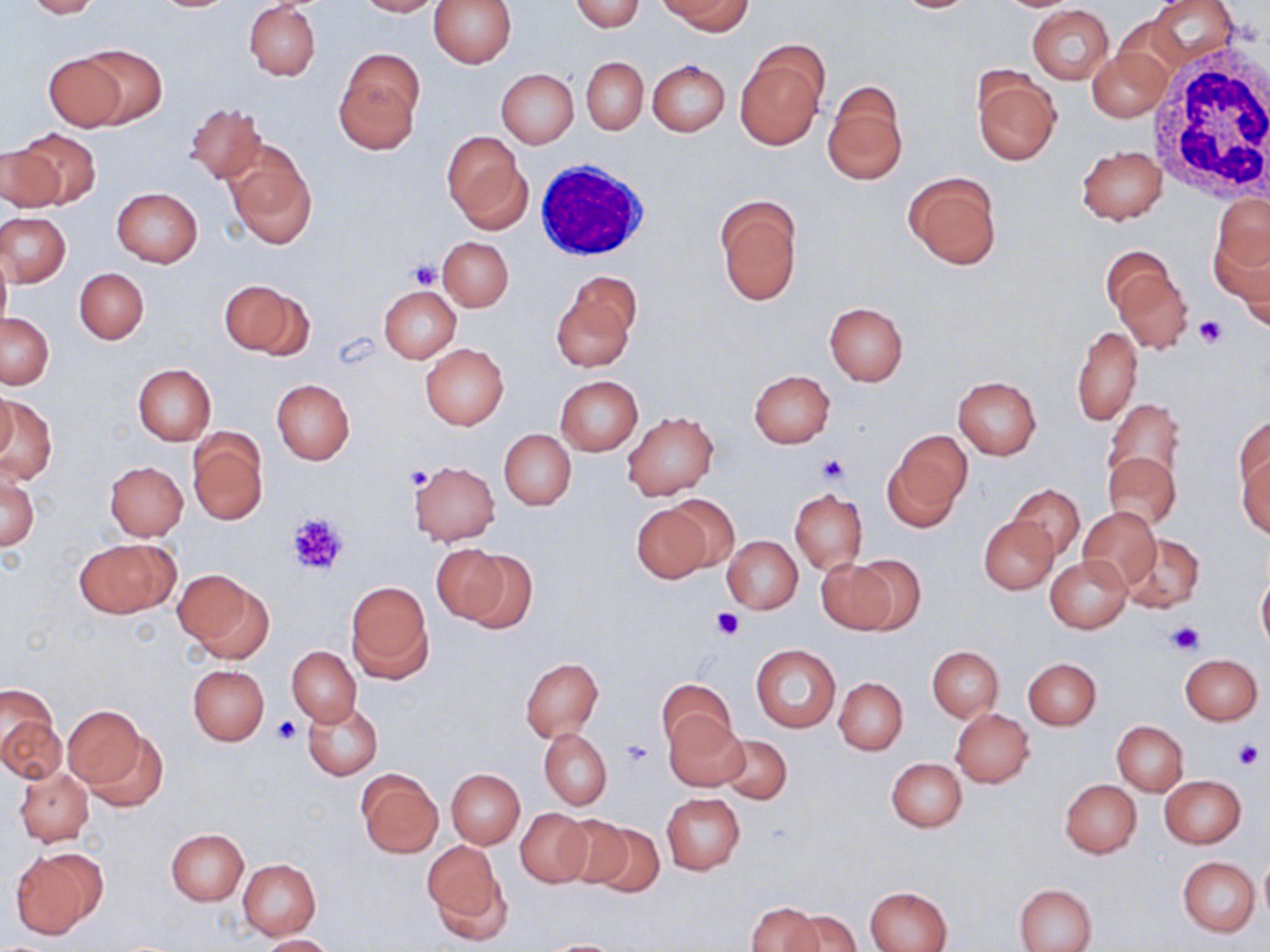
Approximate bounding boxes as (x1, y1, x2, y2) in pixels. Platelet locations: (407, 260, 443, 289), (1193, 313, 1225, 347), (816, 454, 850, 486), (405, 464, 432, 492), (287, 512, 347, 576), (711, 606, 744, 640), (1167, 620, 1204, 656), (274, 715, 303, 746), (620, 738, 654, 768), (1233, 739, 1265, 771). Uninfected red blood cell locations: (24, 0, 102, 18), (358, 0, 437, 17), (429, 0, 516, 66), (571, 0, 646, 32), (662, 0, 750, 34), (892, 0, 978, 13), (1149, 0, 1240, 66), (244, 3, 321, 80), (1027, 4, 1114, 84), (735, 40, 829, 150), (75, 45, 167, 129), (334, 50, 423, 154), (1088, 50, 1172, 122), (41, 52, 128, 131), (581, 57, 648, 134), (647, 60, 729, 135), (497, 69, 578, 147), (972, 69, 1061, 165), (822, 80, 908, 185), (185, 102, 266, 184), (14, 127, 101, 209), (443, 132, 530, 232), (223, 142, 317, 247), (0, 146, 65, 213), (1075, 146, 1167, 225), (903, 172, 1003, 270), (112, 187, 203, 267), (1210, 191, 1269, 287), (715, 195, 802, 306), (2, 212, 71, 287), (439, 237, 513, 311), (0, 249, 10, 334), (1107, 255, 1193, 354), (75, 269, 149, 343), (551, 277, 639, 372), (220, 281, 308, 357), (378, 285, 460, 363), (824, 302, 907, 386), (1, 313, 54, 388), (1072, 325, 1142, 427), (420, 343, 508, 429), (132, 364, 216, 445), (749, 370, 834, 448), (952, 375, 1042, 459), (556, 376, 643, 454), (271, 379, 355, 464), (1, 387, 16, 462), (2, 398, 58, 481), (1104, 399, 1185, 487), (622, 410, 719, 501), (1232, 417, 1268, 499), (187, 428, 268, 524), (499, 428, 575, 511), (884, 430, 971, 529), (1236, 439, 1270, 537), (1104, 452, 1182, 531), (106, 461, 188, 539), (409, 461, 500, 545), (1, 470, 39, 551), (1010, 484, 1084, 559), (790, 489, 867, 573), (660, 495, 741, 573), (631, 500, 716, 581), (1077, 507, 1161, 589), (979, 515, 1058, 593), (1121, 532, 1204, 611), (722, 535, 802, 614), (74, 538, 178, 618), (432, 543, 513, 623), (459, 551, 536, 632), (1045, 555, 1131, 633), (816, 557, 904, 634), (175, 569, 272, 660), (1257, 572, 1270, 654), (345, 582, 432, 681), (751, 644, 840, 732), (288, 646, 361, 726), (928, 646, 1002, 722), (1179, 654, 1262, 725), (520, 657, 604, 741), (1023, 657, 1101, 729), (187, 664, 269, 744), (834, 677, 907, 755), (657, 679, 736, 753), (303, 701, 383, 779), (6, 704, 76, 839), (63, 704, 148, 792), (951, 709, 1034, 787), (664, 713, 750, 792), (2, 715, 67, 782), (1113, 722, 1187, 794), (79, 724, 171, 814), (539, 727, 612, 809), (721, 734, 792, 803), (886, 757, 967, 833), (13, 766, 92, 846), (447, 768, 525, 848), (358, 771, 442, 857), (1160, 776, 1246, 848), (1060, 780, 1141, 858), (661, 792, 745, 874), (515, 807, 594, 887), (548, 813, 634, 893), (578, 817, 665, 897), (167, 829, 249, 905), (422, 841, 508, 937), (9, 847, 104, 938), (1258, 853, 1270, 926), (1178, 856, 1259, 937), (238, 859, 321, 939), (1015, 883, 1096, 952), (866, 886, 952, 952), (747, 902, 820, 952), (786, 909, 862, 952), (259, 934, 335, 952), (537, 938, 630, 951). White blood cell locations: (1151, 49, 1270, 199), (533, 157, 656, 265). Slide-level diagnosis: negative for blood parasites. May-Grünwald-Giemsa-stained preparation. Image is 1270×952 pixels. Optical microscopy. Thin blood film. One field of a larger specimen. 1000x magnification.